Locate every uninfected red blood cell.
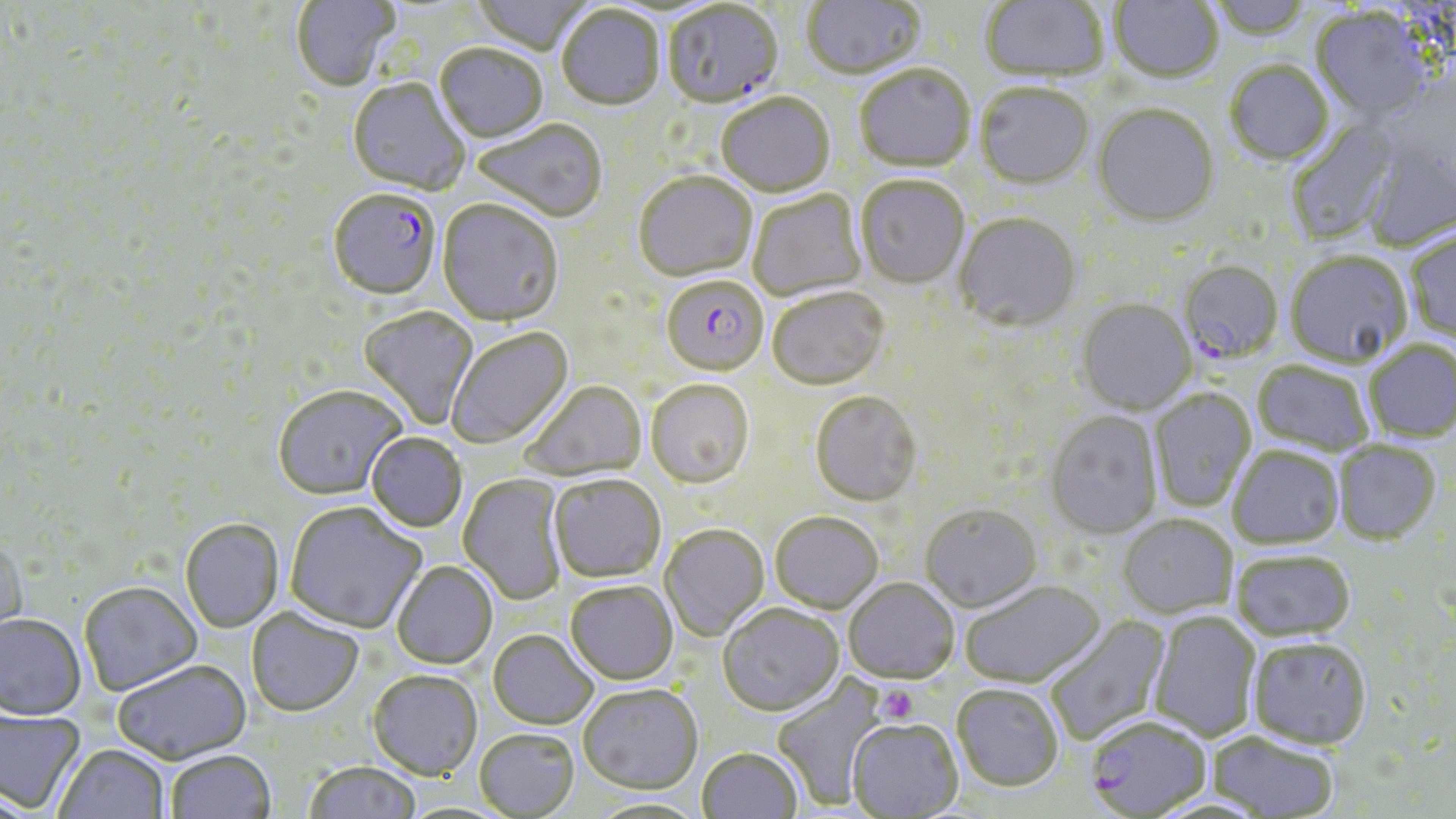
Approximate bounding boxes as (x1, y1, x2, y2) in pixels.
Uninfected red blood cells: (291, 0, 399, 93), (472, 0, 593, 58), (802, 0, 926, 81), (980, 0, 1109, 84), (1110, 0, 1223, 84), (1206, 0, 1315, 42), (557, 7, 665, 112), (1310, 10, 1434, 124), (434, 46, 548, 145), (1226, 62, 1335, 167), (854, 66, 975, 174), (347, 79, 470, 197), (975, 85, 1093, 191), (716, 94, 835, 199), (1092, 106, 1220, 230), (1286, 117, 1402, 243), (472, 120, 607, 224), (1362, 143, 1456, 253), (633, 174, 758, 283), (855, 178, 969, 291), (748, 191, 868, 301), (437, 201, 564, 329), (954, 214, 1082, 334), (1406, 230, 1456, 344), (1285, 253, 1412, 369), (768, 291, 889, 392), (1076, 300, 1196, 416), (359, 307, 479, 430), (446, 327, 574, 449), (1365, 343, 1456, 443), (1252, 362, 1374, 458), (520, 380, 646, 483), (645, 381, 754, 490), (272, 385, 407, 500), (1149, 390, 1256, 512), (810, 392, 922, 509), (1045, 412, 1162, 539), (366, 432, 467, 532), (1333, 441, 1441, 545), (1228, 447, 1344, 549), (458, 474, 569, 606), (549, 474, 666, 583), (285, 502, 426, 634), (919, 505, 1042, 612), (770, 512, 883, 614), (1118, 515, 1237, 618), (179, 518, 284, 633), (661, 525, 769, 641), (0, 539, 27, 654), (1231, 551, 1356, 642), (391, 561, 497, 669), (844, 578, 959, 683), (960, 580, 1105, 688), (79, 581, 201, 696), (565, 581, 678, 685), (717, 604, 843, 717), (246, 608, 363, 717), (1149, 612, 1262, 742), (0, 614, 86, 721), (1043, 614, 1170, 745), (488, 630, 598, 730), (1249, 636, 1372, 749), (112, 660, 251, 764), (368, 670, 482, 780), (771, 676, 888, 810), (952, 683, 1064, 790), (579, 684, 703, 795), (1, 708, 85, 812), (848, 720, 963, 818), (474, 729, 579, 818), (1208, 731, 1339, 818), (53, 744, 170, 819), (697, 748, 802, 819), (166, 749, 276, 819), (303, 761, 421, 819), (585, 796, 710, 818).

Platelet locations: (875, 684, 918, 725). Plasmodium falciparum-infected red blood cell locations: (663, 3, 784, 111), (328, 191, 441, 301), (1177, 262, 1283, 366), (656, 275, 771, 381), (1085, 716, 1212, 817). Slide-level diagnosis: Plasmodium falciparum. May-Grünwald-Giemsa-stained preparation. One field of a larger specimen. Thin blood smear. Image is 1456×819 pixels. Light microscopy. Captured at 1000x magnification.